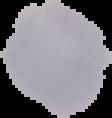
Summary:
  - Malaria status: uninfected
  - Image type: segmented cell region with the area outside set to black
  - Preparation: thin blood film
  - Image size: 112×118 pixels